State which parasite is depicted.
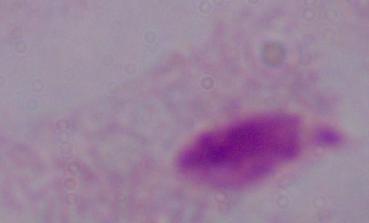

This is a trichomonad.

Micrograph. 1000x magnification.